Locate Plasmodium parasites and leukocytes.
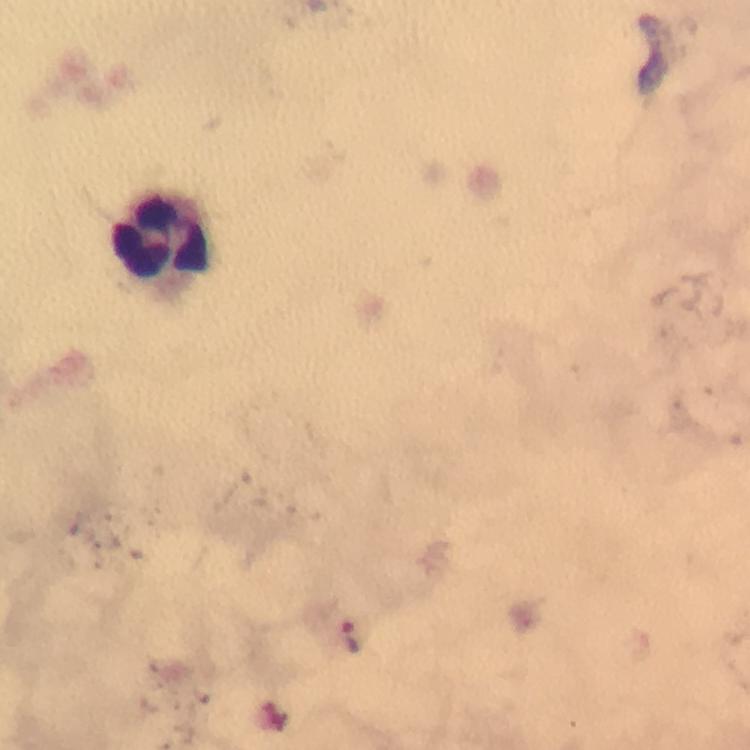

Approximate centers as {x, y} in pixels.
Plasmodium parasites: {657, 52}.
Leukocytes: {164, 240}.

Immersion oil was used. Image is 750×750 pixels. Photographed through the microscope with a smartphone camera. Giemsa-stained preparation. From a malaria diagnostic workup. A crop from one field of view. Thick blood film. 100x magnification.